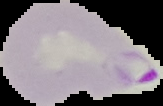
preparation = thin blood film
malaria status = parasitized
image type = segmented cell region with the area outside set to black
image size = 163×106 pixels